Name the blood parasite species.
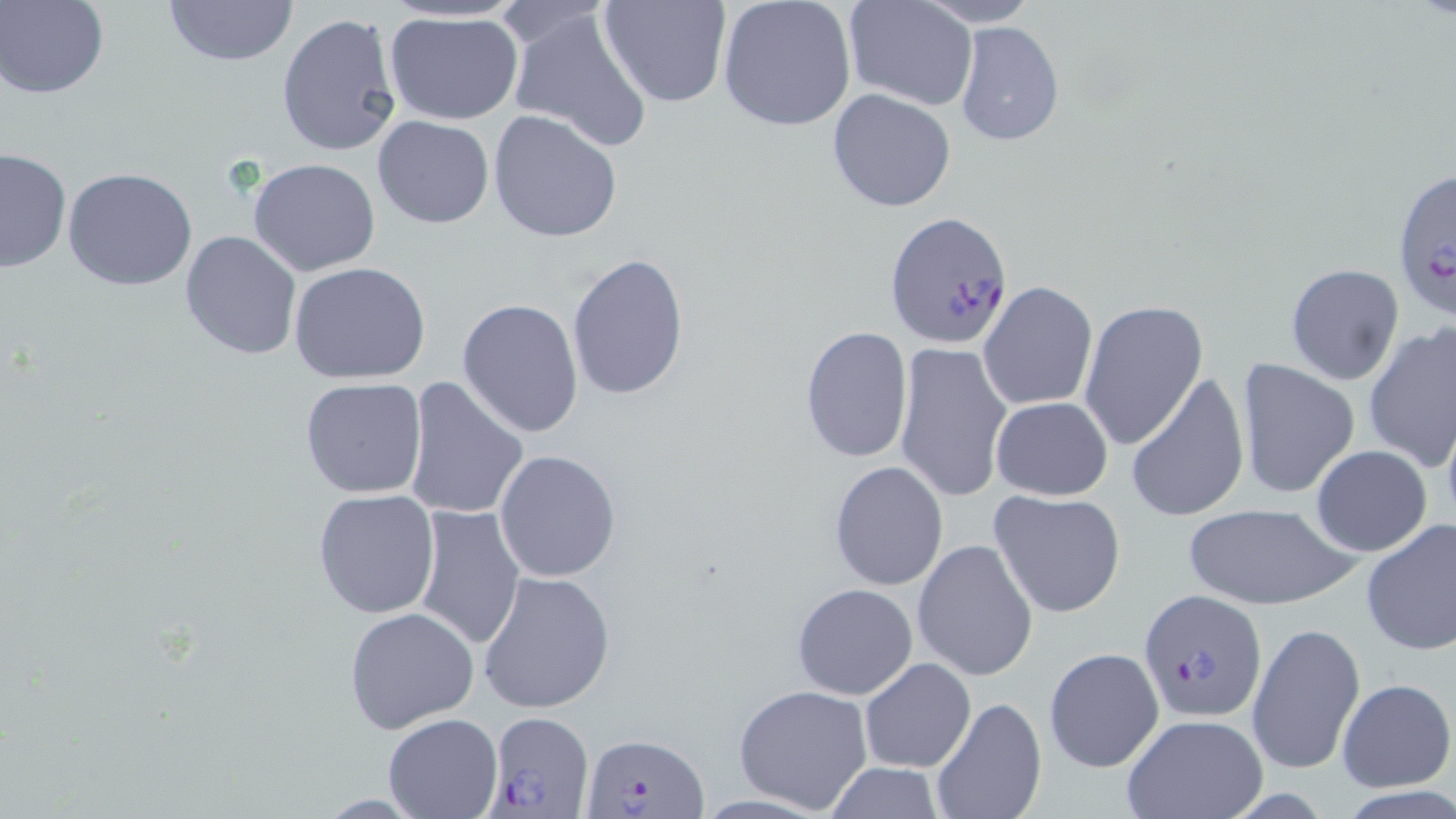

Plasmodium falciparum.

Summary:
  - Coordinate format: approximate bounding boxes as [x1, y1, x2, y2] in pixels
  - Plasmodium falciparum-infected red blood cell locations: [1391, 165, 1456, 319], [884, 209, 1014, 348], [1137, 589, 1267, 723], [485, 711, 594, 818], [584, 730, 707, 817]
  - Uninfected red blood cell locations: [2, 0, 108, 98], [160, 0, 300, 68], [599, 0, 731, 108], [716, 0, 858, 132], [843, 0, 979, 112], [915, 1, 1042, 27], [504, 5, 654, 151], [385, 11, 525, 127], [277, 12, 402, 158], [954, 20, 1065, 148], [827, 87, 958, 212], [488, 110, 623, 245], [372, 115, 494, 228], [0, 147, 71, 274], [248, 157, 381, 277], [62, 167, 198, 291], [180, 228, 304, 361], [566, 250, 691, 401], [290, 262, 432, 385], [1284, 262, 1405, 387], [978, 281, 1098, 411], [457, 298, 584, 439], [1079, 300, 1208, 450], [1362, 322, 1455, 476], [799, 325, 913, 464], [894, 341, 1013, 504], [1235, 357, 1361, 499], [1125, 370, 1250, 525], [299, 377, 429, 500], [404, 377, 529, 522], [990, 396, 1114, 501], [1310, 445, 1434, 557], [493, 449, 623, 581], [828, 460, 948, 591], [312, 488, 441, 620], [988, 489, 1127, 617], [1184, 502, 1354, 609], [411, 505, 526, 652], [1360, 518, 1456, 655], [913, 539, 1039, 681], [476, 570, 616, 714], [792, 582, 918, 700], [345, 606, 479, 735], [1247, 620, 1364, 777], [1042, 646, 1165, 774], [859, 659, 976, 771], [1336, 678, 1454, 791], [733, 683, 875, 815], [928, 695, 1046, 819], [383, 711, 503, 818], [1120, 714, 1269, 819], [823, 763, 947, 818]
  - Image size: 1456×819 pixels
  - Modality: light microscopy
  - Stain: May-Grünwald-Giemsa
  - Magnification: 1000x
  - Field of view: one of a larger specimen
  - Preparation: thin blood film